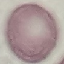 Malaria status: uninfected. Giemsa-stained preparation. Thin smear of blood. Automatically extracted cell patch, resized to 64 × 64 pixels. Photographed with a smartphone camera at the microscope eyepiece.